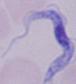

identification = trypanosome
modality = photomicrograph
magnification = 1000x